Assess this cell for malaria.
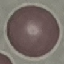

It is uninfected.

{
  "capture": "smartphone camera at the microscope eyepiece",
  "image_type": "automatically extracted cell patch, resized to 64 × 64 pixels",
  "preparation": "thin blood smear",
  "stain": "Giemsa"
}